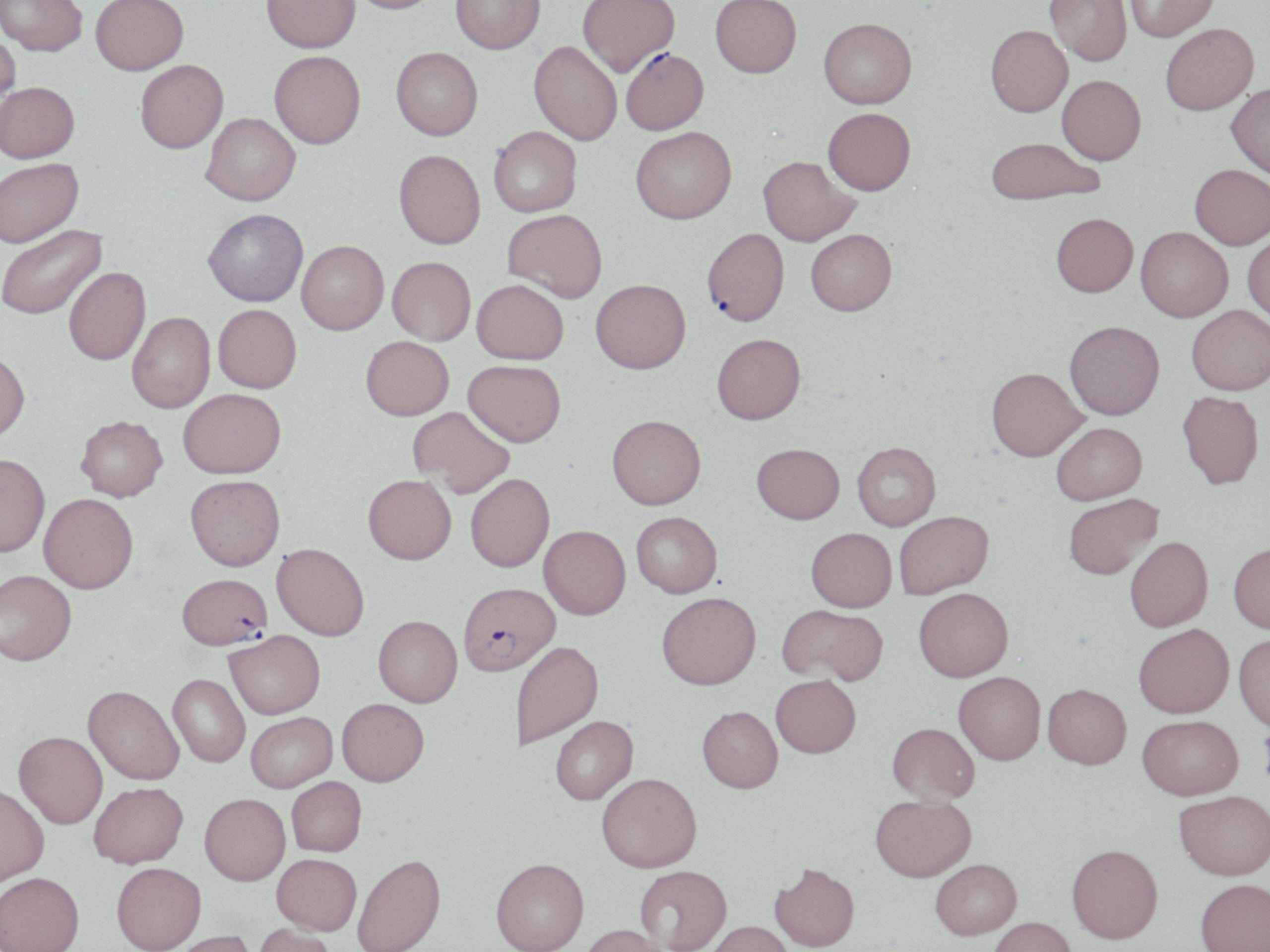

slide-level diagnosis = Plasmodium falciparum
uninfected red blood cell locations = approximate bounding boxes as named x1/y1/x2/y2 corners in pixels: (x1=0, y1=0, x2=87, y2=60), (x1=91, y1=0, x2=188, y2=78), (x1=261, y1=0, x2=361, y2=56), (x1=345, y1=0, x2=440, y2=18), (x1=451, y1=0, x2=545, y2=57), (x1=577, y1=0, x2=680, y2=80), (x1=1045, y1=0, x2=1131, y2=69), (x1=1124, y1=0, x2=1220, y2=44), (x1=710, y1=1, x2=802, y2=81), (x1=819, y1=23, x2=917, y2=113), (x1=1161, y1=26, x2=1259, y2=119), (x1=985, y1=28, x2=1073, y2=120), (x1=0, y1=31, x2=21, y2=123), (x1=528, y1=43, x2=621, y2=148), (x1=391, y1=51, x2=483, y2=145), (x1=269, y1=54, x2=366, y2=153), (x1=136, y1=63, x2=229, y2=157), (x1=1057, y1=78, x2=1145, y2=169), (x1=0, y1=85, x2=80, y2=167), (x1=1225, y1=86, x2=1270, y2=185), (x1=823, y1=112, x2=915, y2=200), (x1=200, y1=115, x2=301, y2=210), (x1=489, y1=129, x2=582, y2=220), (x1=631, y1=130, x2=737, y2=229), (x1=986, y1=141, x2=1102, y2=210), (x1=392, y1=153, x2=486, y2=253), (x1=757, y1=159, x2=860, y2=249), (x1=0, y1=161, x2=86, y2=252), (x1=1190, y1=168, x2=1270, y2=254), (x1=203, y1=211, x2=308, y2=310), (x1=503, y1=212, x2=607, y2=305), (x1=1051, y1=217, x2=1138, y2=302), (x1=1, y1=225, x2=109, y2=323), (x1=1135, y1=230, x2=1233, y2=325), (x1=806, y1=233, x2=897, y2=321), (x1=1242, y1=235, x2=1270, y2=328), (x1=297, y1=243, x2=389, y2=338), (x1=387, y1=259, x2=475, y2=348), (x1=64, y1=269, x2=151, y2=368), (x1=471, y1=283, x2=568, y2=368), (x1=591, y1=283, x2=691, y2=378), (x1=213, y1=306, x2=302, y2=395), (x1=1187, y1=309, x2=1270, y2=399), (x1=127, y1=314, x2=216, y2=415), (x1=1065, y1=325, x2=1165, y2=424), (x1=360, y1=338, x2=453, y2=422), (x1=712, y1=338, x2=805, y2=428), (x1=0, y1=352, x2=30, y2=446), (x1=463, y1=362, x2=565, y2=450), (x1=986, y1=371, x2=1088, y2=465), (x1=178, y1=389, x2=286, y2=478), (x1=1177, y1=394, x2=1264, y2=493), (x1=408, y1=407, x2=514, y2=498), (x1=75, y1=416, x2=168, y2=501), (x1=607, y1=418, x2=705, y2=513), (x1=1052, y1=425, x2=1147, y2=506), (x1=852, y1=443, x2=940, y2=531), (x1=751, y1=444, x2=845, y2=525), (x1=0, y1=454, x2=50, y2=557), (x1=465, y1=473, x2=555, y2=573), (x1=185, y1=474, x2=285, y2=571), (x1=363, y1=474, x2=456, y2=564), (x1=39, y1=493, x2=139, y2=593), (x1=1064, y1=494, x2=1164, y2=581), (x1=894, y1=512, x2=994, y2=599), (x1=631, y1=513, x2=722, y2=600), (x1=538, y1=526, x2=630, y2=620), (x1=805, y1=528, x2=897, y2=613), (x1=1125, y1=536, x2=1214, y2=632), (x1=272, y1=543, x2=369, y2=641), (x1=1229, y1=544, x2=1270, y2=635), (x1=0, y1=570, x2=76, y2=665), (x1=914, y1=588, x2=1013, y2=682), (x1=657, y1=594, x2=761, y2=693), (x1=777, y1=604, x2=887, y2=686), (x1=374, y1=615, x2=462, y2=708), (x1=1133, y1=624, x2=1233, y2=719), (x1=225, y1=630, x2=325, y2=718), (x1=1233, y1=634, x2=1270, y2=733), (x1=512, y1=642, x2=604, y2=750), (x1=953, y1=672, x2=1045, y2=766), (x1=168, y1=673, x2=250, y2=768), (x1=771, y1=675, x2=861, y2=759), (x1=83, y1=685, x2=184, y2=784), (x1=1043, y1=685, x2=1131, y2=772), (x1=337, y1=698, x2=429, y2=786), (x1=697, y1=707, x2=783, y2=796), (x1=246, y1=711, x2=337, y2=792), (x1=551, y1=716, x2=638, y2=806), (x1=1137, y1=717, x2=1243, y2=803), (x1=887, y1=723, x2=980, y2=805), (x1=14, y1=731, x2=107, y2=828), (x1=597, y1=773, x2=701, y2=875), (x1=286, y1=776, x2=366, y2=856), (x1=89, y1=782, x2=188, y2=868), (x1=0, y1=783, x2=49, y2=887), (x1=1173, y1=791, x2=1270, y2=883), (x1=200, y1=792, x2=290, y2=884), (x1=869, y1=794, x2=977, y2=882), (x1=1066, y1=844, x2=1163, y2=944), (x1=272, y1=853, x2=361, y2=934), (x1=353, y1=853, x2=446, y2=951), (x1=491, y1=858, x2=588, y2=952), (x1=931, y1=858, x2=1021, y2=939), (x1=112, y1=862, x2=206, y2=952), (x1=769, y1=863, x2=859, y2=951), (x1=635, y1=866, x2=731, y2=951), (x1=0, y1=872, x2=84, y2=952), (x1=1196, y1=879, x2=1270, y2=952), (x1=988, y1=916, x2=1075, y2=952), (x1=703, y1=922, x2=791, y2=952), (x1=253, y1=924, x2=337, y2=952), (x1=579, y1=925, x2=671, y2=952), (x1=167, y1=930, x2=257, y2=952)
stain = May-Grünwald-Giemsa
preparation = thin blood smear
magnification = 1000x
image size = 1270×952 pixels
modality = optical microscopy
Plasmodium falciparum-infected red blood cell locations = approximate bounding boxes as named x1/y1/x2/y2 corners in pixels: (x1=621, y1=51, x2=710, y2=138), (x1=702, y1=231, x2=790, y2=330), (x1=177, y1=573, x2=273, y2=650), (x1=458, y1=582, x2=560, y2=677)
field of view = one of a larger specimen